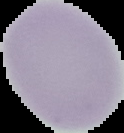

Result: no malaria parasites seen. Cell region segmented out of the field of view; the surrounding area is masked to black. Image is 124×133 pixels. From a thin blood smear.